Find the cells and give the type of each one.
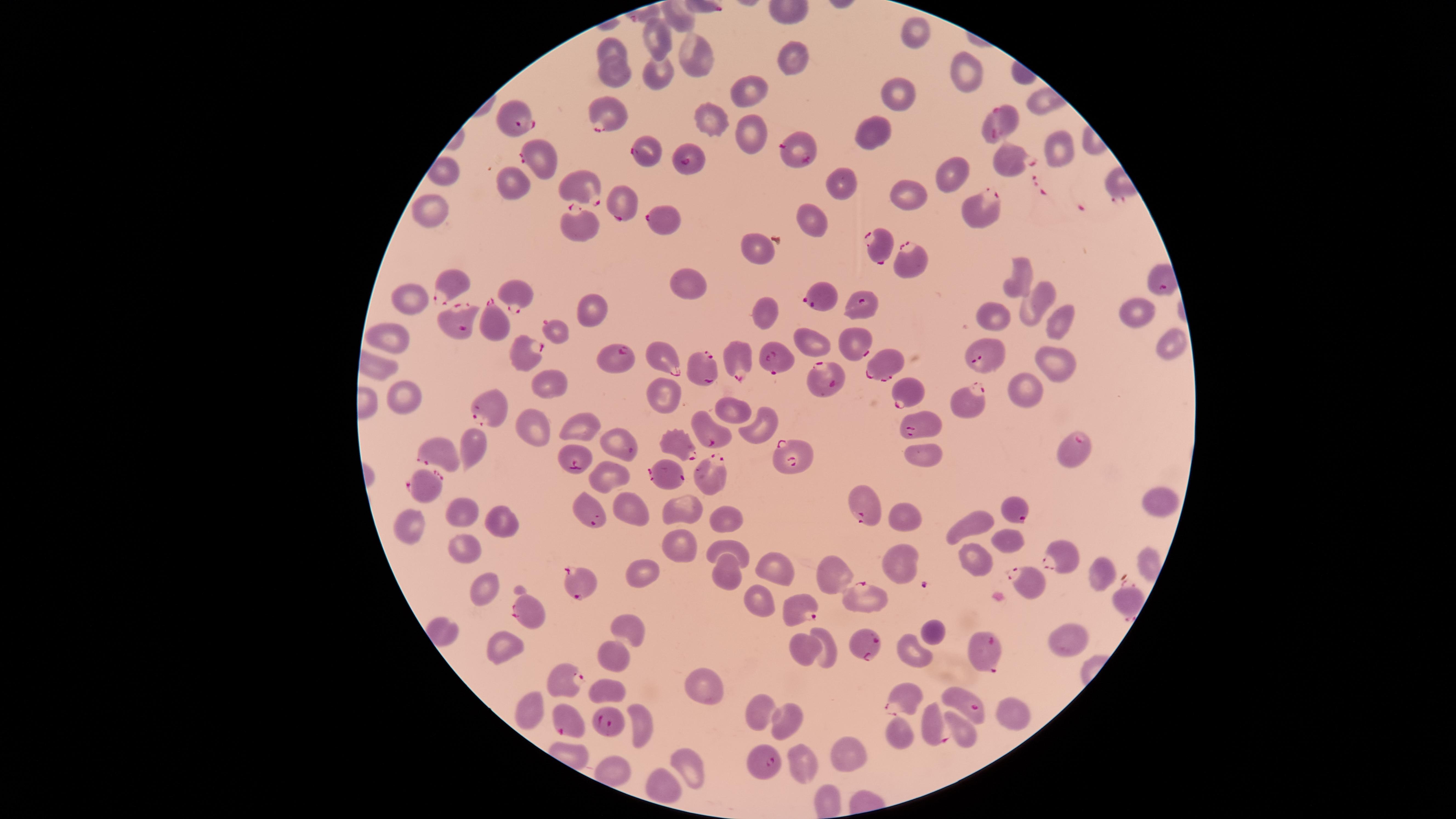
Approximate marker points as [x, y] in pixels.
Parasitized RBCs: [607, 116], [513, 117], [1000, 119], [646, 150], [797, 152], [544, 159], [1008, 159], [692, 163], [583, 184], [625, 201], [986, 206], [661, 217], [579, 224], [881, 244], [914, 259], [453, 287], [519, 294], [822, 296], [862, 309], [455, 323], [494, 325], [555, 330], [664, 353], [857, 353], [774, 354], [523, 356], [982, 356], [620, 358], [735, 359], [704, 365], [878, 365], [830, 379], [906, 390], [968, 397], [490, 408], [918, 426], [710, 437], [619, 443], [1070, 444], [683, 448], [438, 449], [794, 455], [576, 457], [709, 469], [667, 474], [421, 482], [861, 500], [1014, 508], [590, 512], [1060, 560], [1028, 579], [582, 588], [1123, 599], [862, 600], [801, 608], [530, 611], [867, 641], [981, 651], [563, 674], [906, 701], [970, 701], [614, 723], [568, 725], [931, 726], [761, 763].
Uninfected RBCs: [912, 33], [656, 38], [615, 50], [696, 58], [793, 61], [613, 73], [963, 74], [657, 75], [902, 89], [746, 94], [715, 121], [876, 128], [753, 133], [1055, 147], [442, 172], [948, 173], [515, 180], [842, 183], [906, 196], [430, 205], [814, 220], [758, 248], [1014, 273], [686, 281], [408, 297], [1032, 303], [589, 309], [1140, 310], [768, 313], [998, 316], [1058, 317], [394, 337], [811, 340], [1166, 345], [1056, 358], [551, 382], [1025, 385], [400, 394], [661, 398], [732, 410], [582, 421], [756, 426], [526, 428], [471, 442], [926, 453], [605, 475], [1159, 503], [635, 507], [460, 511], [686, 511], [726, 515], [500, 519], [908, 519], [403, 522], [971, 523], [1006, 537], [679, 543], [460, 545], [734, 546], [975, 560], [897, 563], [777, 567], [1098, 570], [644, 571], [721, 575], [830, 575], [484, 589], [758, 602], [630, 622], [928, 628], [439, 633], [1064, 638], [502, 640], [828, 642], [911, 646], [804, 648], [616, 656], [610, 689], [700, 695], [531, 702], [528, 705], [1016, 708], [761, 710], [787, 716], [639, 730], [898, 733], [838, 754], [802, 761], [685, 762], [616, 767], [655, 786], [824, 794].
No WBCs identified.

Image is 1456×819 pixels. Thin smear of blood. Species: Plasmodium falciparum. Giemsa-stained preparation. The visible region is circular. One field of view of the specimen. Photographed with a smartphone camera through the microscope eyepiece.